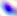

Photomicrograph. 400x magnification. Toxoplasma gondii is seen.